Report the malaria status of this cell.
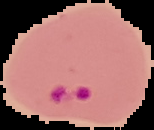
Parasitized.

image type = cell region segmented out of the field of view; surrounding area masked to black
image size = 154×130 pixels
preparation = thin blood film